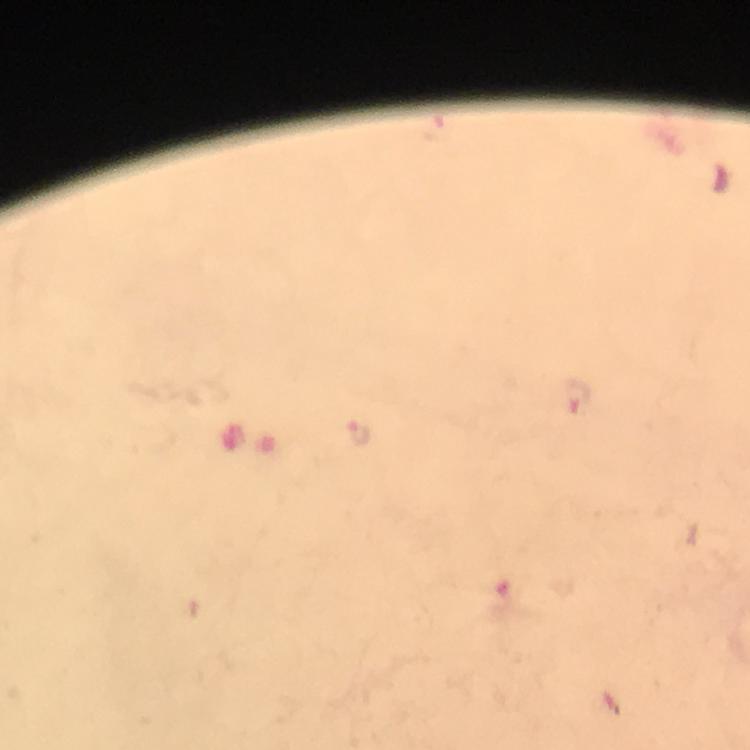

Approximate object centers, in pixels from the top-left corner. Plasmodium parasite locations: (x=577, y=397), (x=358, y=432), (x=503, y=596). Image is 750×750 pixels. Immersion oil applied. 100x magnification. Photographed through the microscope with a smartphone camera. Giemsa stain. From a diagnostic examination for malaria. Thick blood film. Cropped region of a single field of view.